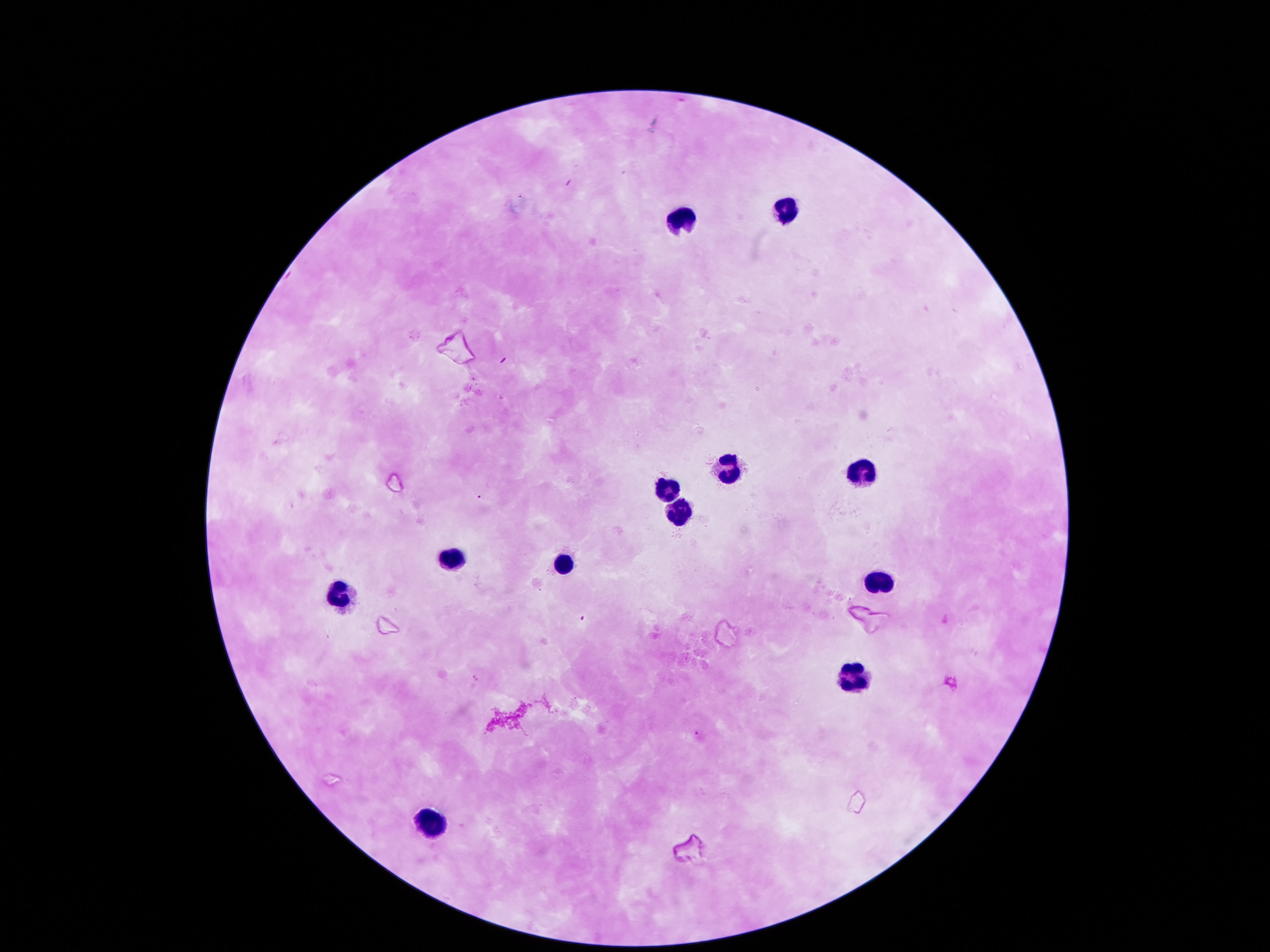

Approximate object centers, in pixels from the top-left corner. Leukocyte locations: (x=787, y=208), (x=681, y=217), (x=722, y=462), (x=855, y=469), (x=668, y=488), (x=677, y=513), (x=448, y=556), (x=561, y=563), (x=881, y=578), (x=338, y=597), (x=852, y=673), (x=425, y=821). Patient malaria status: negative. Giemsa stain. Single field of view. 100x magnification. Thick blood smear. Smartphone photograph taken through the microscope eyepiece. Image is 1270×952 pixels.